Comment on the morphology of the red blood cells.
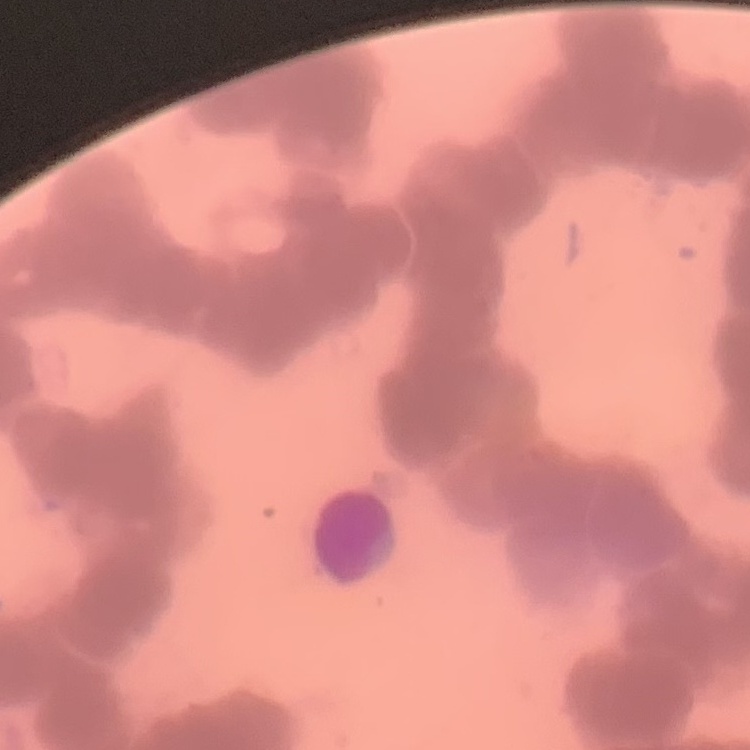

Rouleaux formation.

{
  "preparation": "thin blood film",
  "stain": "Field's or Giemsa",
  "image_type": "one tile cut from a larger photomicrograph"
}